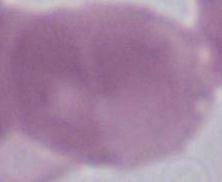

magnification = 1000x
identification = red blood cell
modality = micrograph